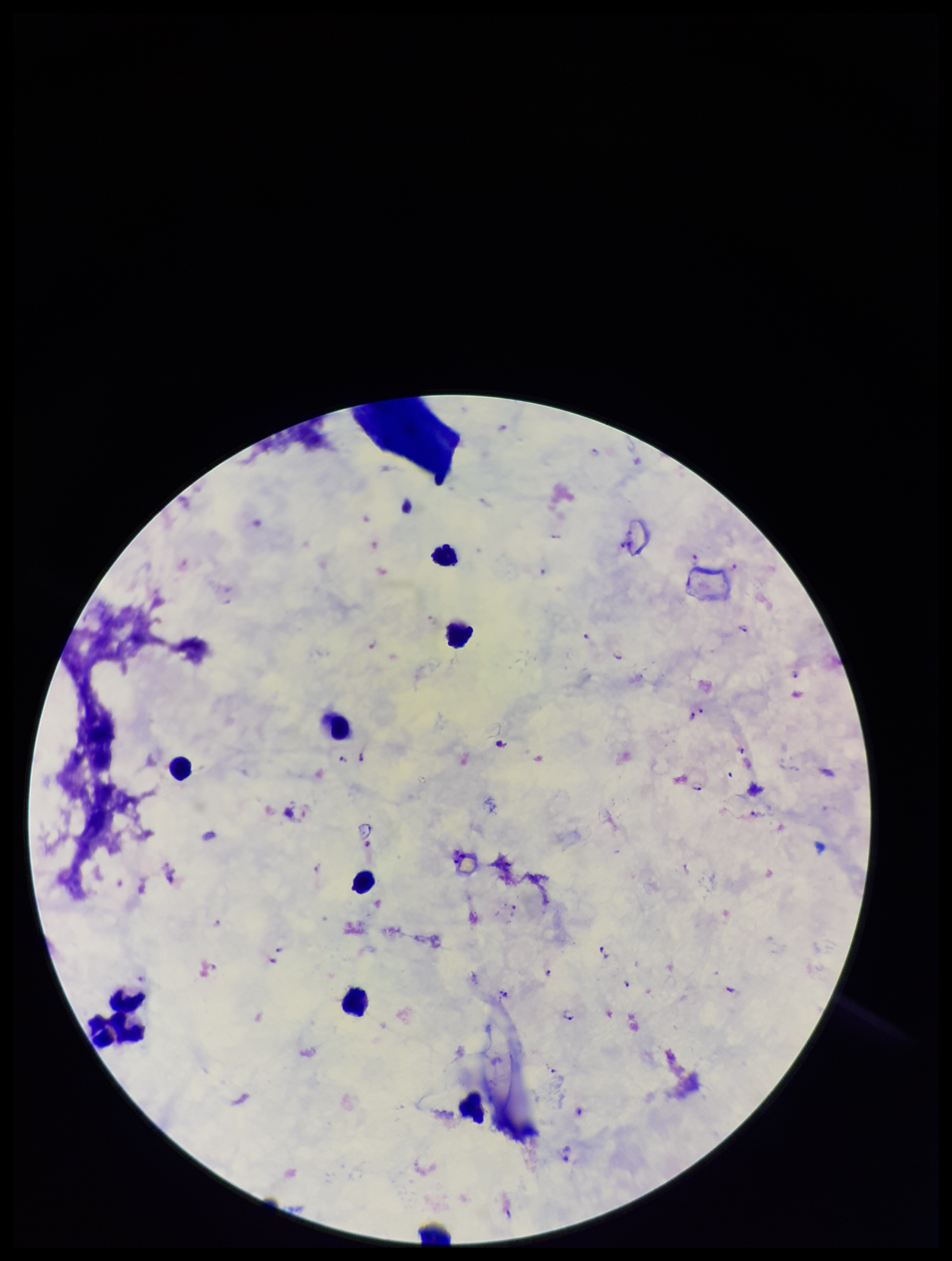 Patient malaria status: infected. Preparation: thick blood smear. One field from this slide. Parasite count: 19. Leukocyte count: 10. Image is 952×1261 pixels. Smartphone photograph taken through the eyepiece of a microscope. Giemsa stain. Species reported for this patient: Plasmodium falciparum. Plasmodium parasites: detected.